Assess this cell for malaria.
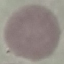
It is uninfected.

Summary:
  - Capture: smartphone camera at the microscope eyepiece
  - Stain: Giemsa
  - Image type: cell patch, automatically extracted from a larger field of view and resized to 64 × 64 pixels
  - Preparation: thin blood smear